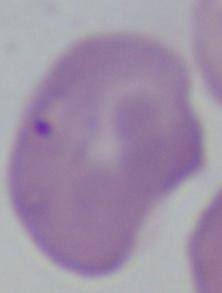
Summary:
  - Magnification: 1000x
  - Identification: Babesia
  - Modality: micrograph